Outline each Plasmodium falciparum-infected red blood cell.
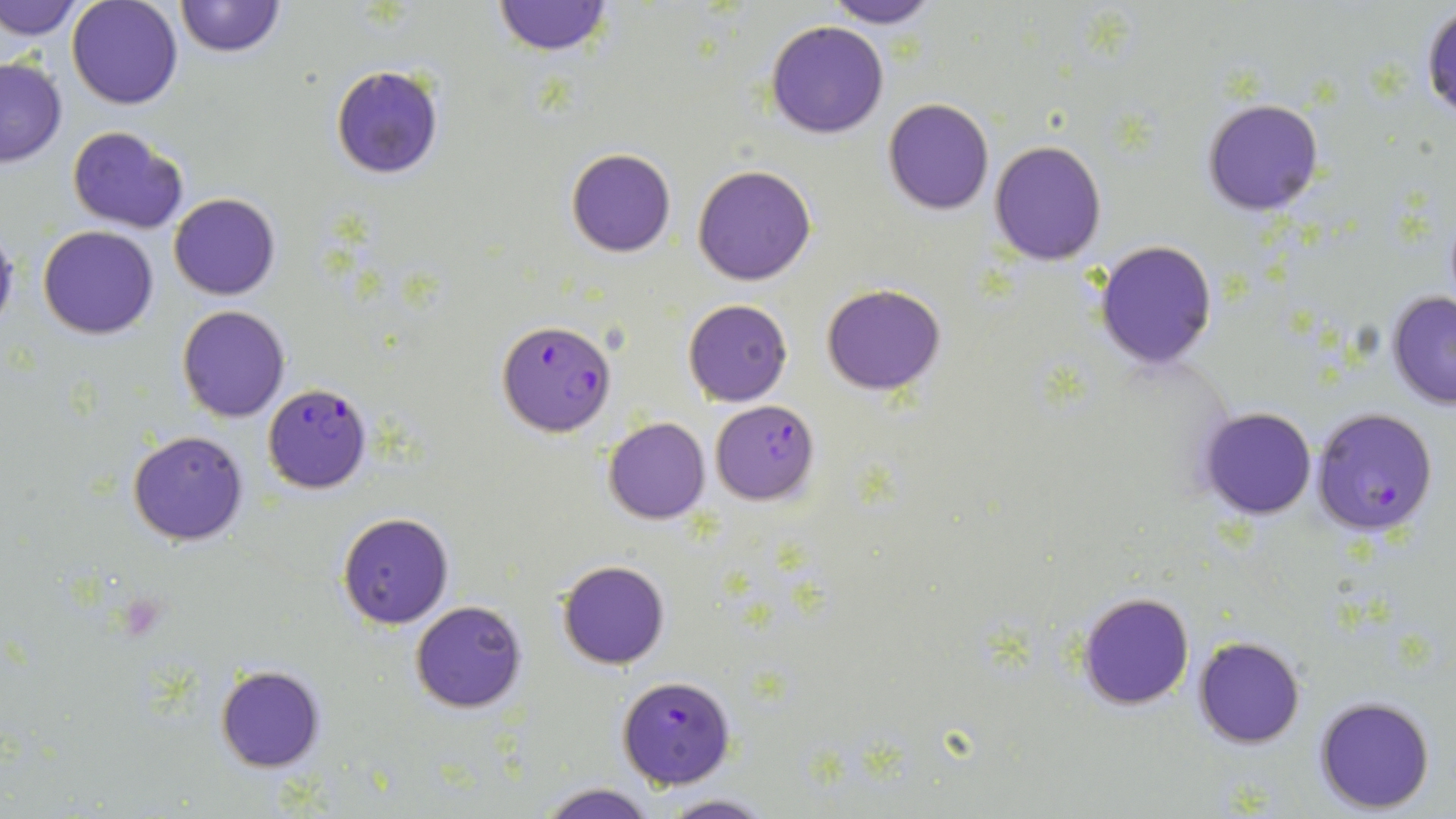
Approximate bounding boxes as (x1,y1)-(x2,y2) corner pairs in pixels.
Plasmodium falciparum-infected red blood cells: (496,320)-(617,436), (262,381)-(373,494), (711,399)-(820,505), (1310,407)-(1439,536), (619,676)-(736,789).

Uninfected red blood cell locations: (0,0)-(85,42), (67,0)-(182,109), (172,0)-(286,58), (492,0)-(613,57), (821,0)-(941,28), (1421,4)-(1455,120), (766,20)-(889,139), (0,56)-(68,166), (331,65)-(445,180), (883,99)-(995,216), (1204,99)-(1324,216), (68,126)-(191,233), (989,140)-(1107,266), (566,149)-(676,257), (693,163)-(816,286), (168,191)-(280,299), (0,224)-(19,338), (39,225)-(159,339), (1093,239)-(1218,371), (824,284)-(946,395), (1387,290)-(1456,411), (682,300)-(792,407), (177,306)-(290,423), (1198,406)-(1318,520), (604,417)-(710,524), (128,429)-(250,546), (338,512)-(454,629), (557,559)-(671,670), (1078,592)-(1194,710), (409,601)-(527,714), (1193,635)-(1306,748), (215,665)-(326,772), (1315,695)-(1436,813), (535,781)-(657,819), (654,794)-(775,818). Slide-level diagnosis: Plasmodium falciparum. Thin blood smear. One field of a larger specimen. Captured at 1000x magnification. Optical microscopy. May-Grünwald-Giemsa stain. Image is 1456×819 pixels.